Point out each malaria parasite and each leukocyte.
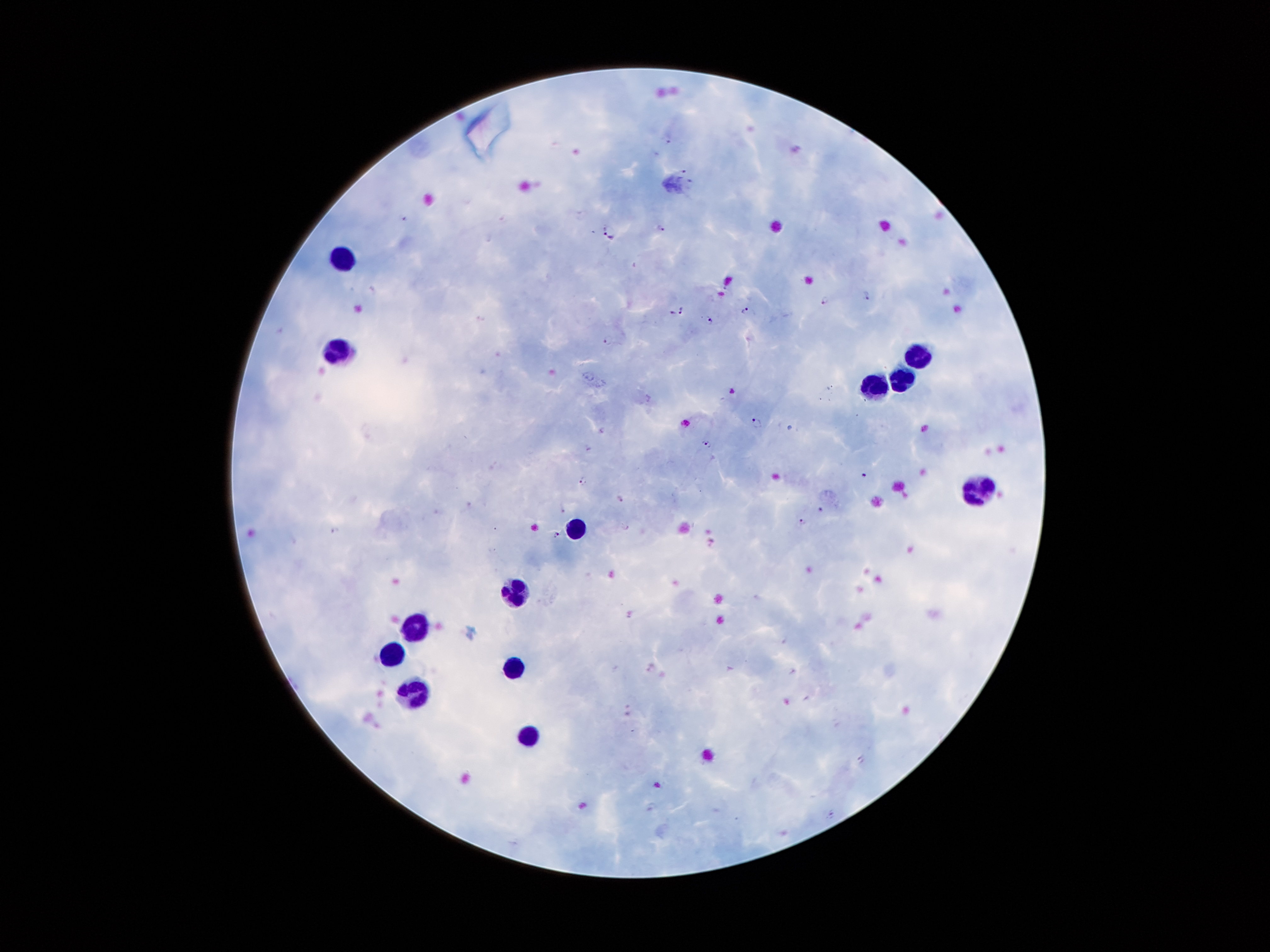
Approximate centers as [x, y] in pixels.
Malaria parasites: [670, 140], [684, 169], [691, 183], [660, 229], [611, 231], [866, 294], [824, 300], [681, 310], [746, 310], [708, 319], [609, 339], [757, 422], [706, 444], [866, 476], [584, 481], [621, 498], [822, 509], [802, 522], [334, 531], [557, 535], [652, 807], [833, 814].
Leukocytes: [338, 259], [340, 350], [916, 355], [907, 383], [875, 385], [977, 491], [578, 522], [521, 593], [412, 625], [395, 660], [514, 666], [411, 689], [528, 739].

Smartphone photograph taken through the microscope eyepiece. Giemsa-stained preparation. Patient malaria status: infected with Plasmodium falciparum. Thick blood film. Image is 1270×952 pixels. Single field of view. 100x magnification.